Assess this cell for malaria.
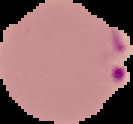
It is parasitized.

{
  "image_type": "cell region segmented out of the field of view; surrounding area masked to black",
  "preparation": "thin blood film",
  "image_size": "133×124 pixels"
}